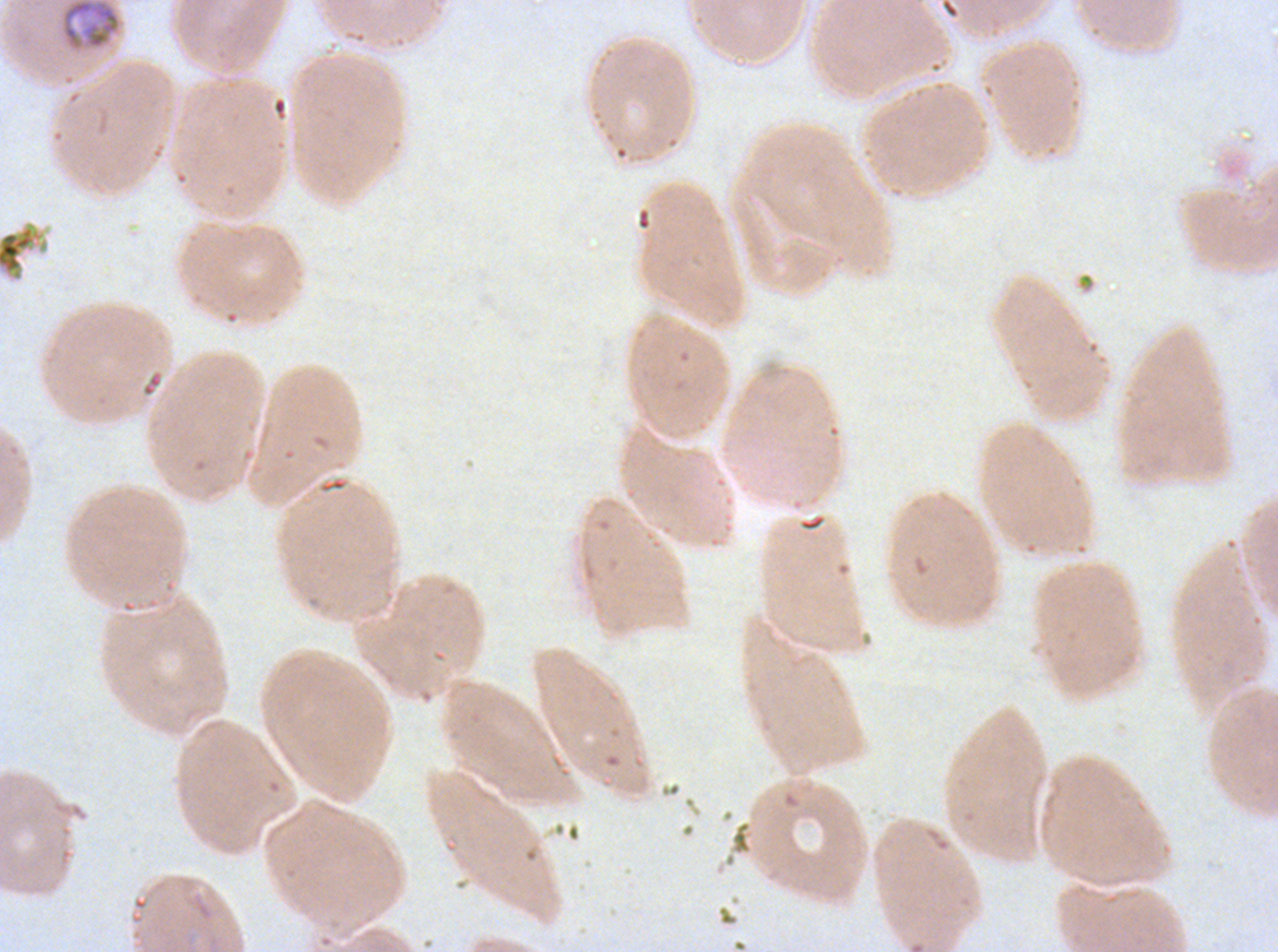

notation = approximate bounding boxes as (x1, y1, x2, y2) in pixels
debris locations = (0, 224, 50, 283)
mid trophozoite locations = (61, 0, 121, 52)
preparation = thin blood film
field of view = sub-image separated from a larger composite
stain = Giemsa
image size = 1278×952 pixels
specimen = P. falciparum cultured ex vivo for 24 to 48 hours, from a patient in The Gambia